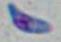

Summary:
  - Modality: micrograph
  - Identification: Toxoplasma gondii
  - Magnification: 1000x